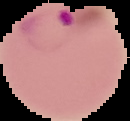

Summary:
  - Preparation: thin blood film
  - Malaria status: parasitized
  - Image size: 130×121 pixels
  - Image type: segmented cell region with the area outside set to black